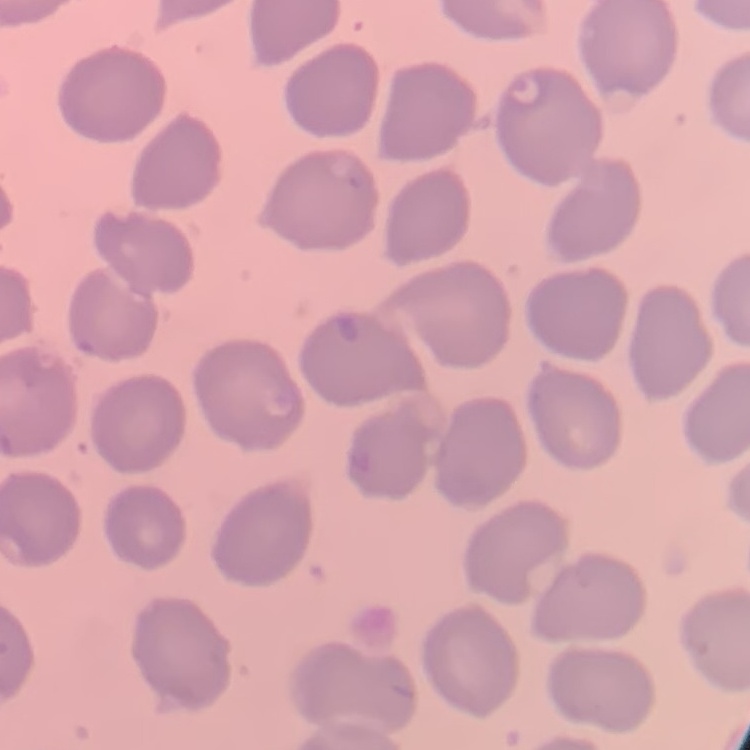
erythrocyte morphology = no rouleaux formation
image type = square crop of a larger photomicrograph
preparation = thin blood film
stain = Field's or Giemsa